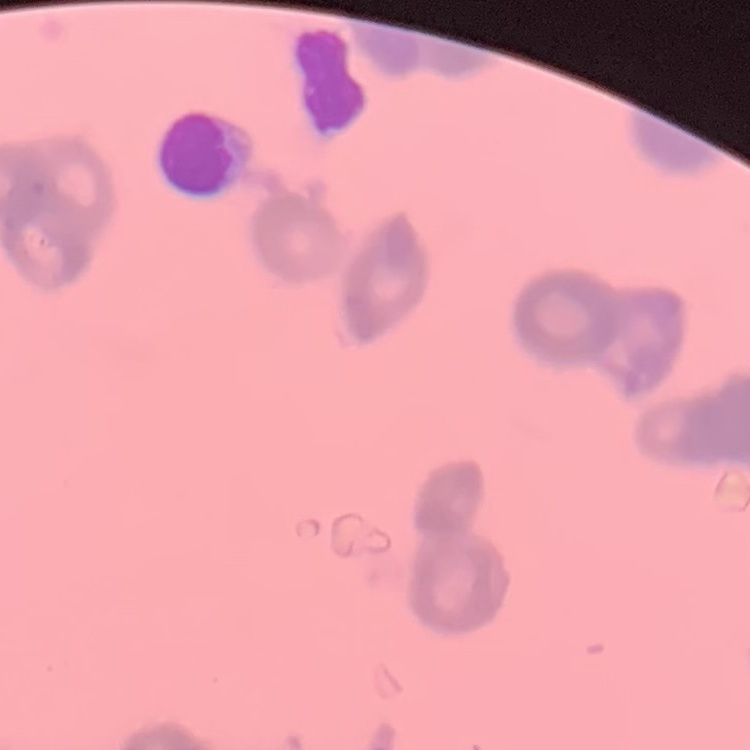
erythrocyte morphology = rouleaux formation
stain = Field's or Giemsa
preparation = thin peripheral smear
image type = square crop of a larger photomicrograph